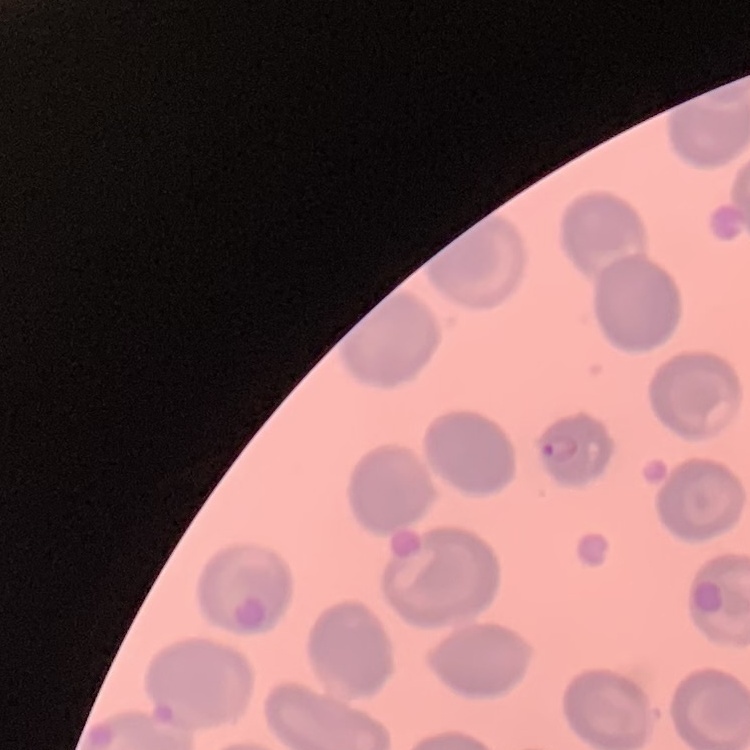

Summary:
  - Erythrocyte morphology: no rouleaux formation
  - Stain: Field's or Giemsa
  - Preparation: thin blood film
  - Image type: one tile cut from a larger photomicrograph